Locate every uninfected red blood cell.
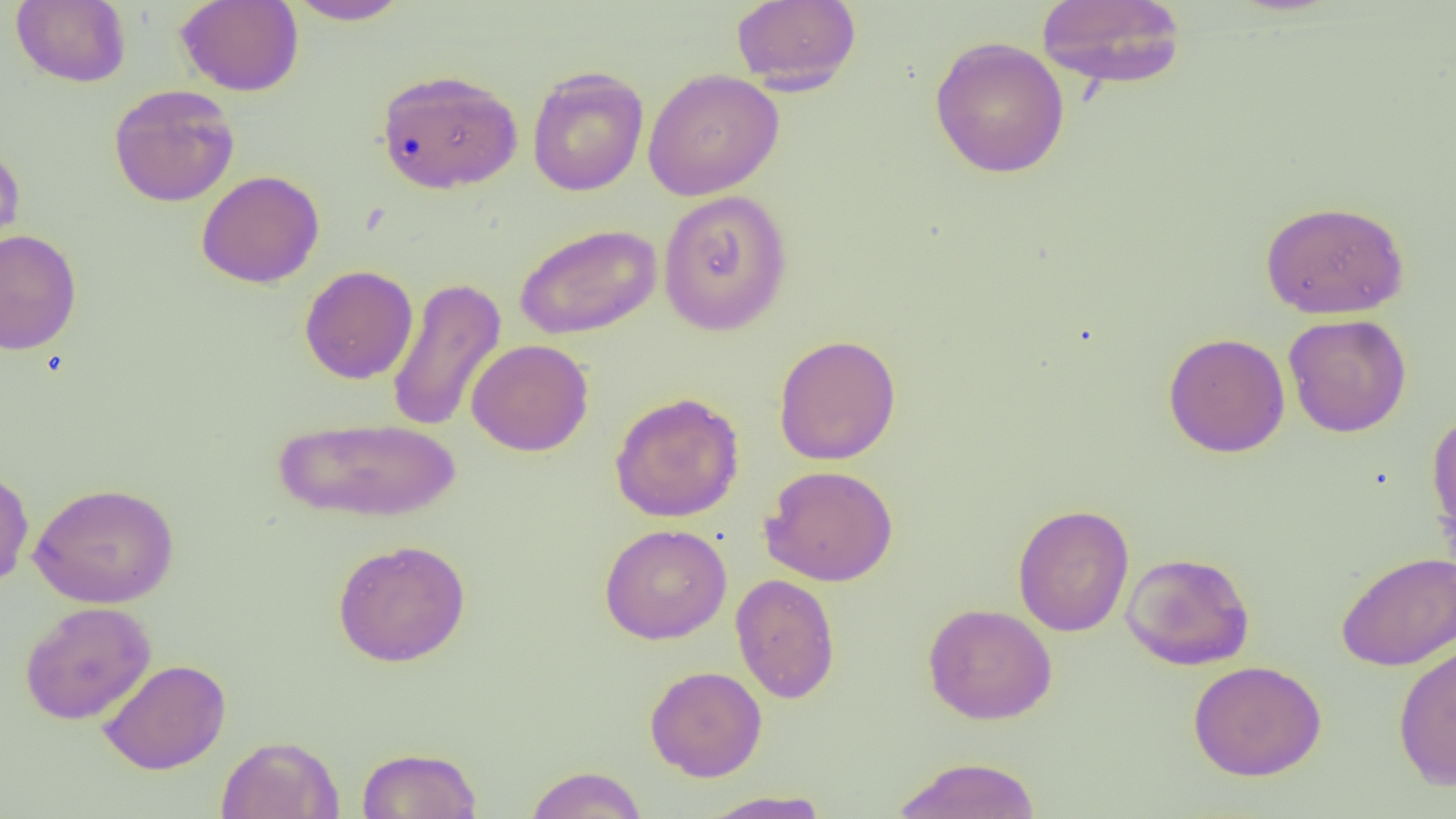
Approximate bounding boxes as (x1,y1)-(x2,y2) corner pairs in pixels.
Uninfected red blood cells: (11,0)-(131,88), (174,0)-(304,97), (284,0)-(413,25), (1035,0)-(1187,89), (731,1)-(861,92), (929,36)-(1070,179), (526,66)-(649,197), (376,68)-(523,195), (642,68)-(784,201), (108,84)-(240,207), (0,142)-(25,259), (196,170)-(325,288), (657,190)-(793,335), (1260,199)-(1410,319), (514,223)-(662,340), (0,229)-(83,356), (299,265)-(418,384), (386,276)-(506,434), (1283,313)-(1412,437), (1163,332)-(1291,457), (774,334)-(902,465), (466,338)-(594,457), (609,391)-(745,523), (1426,410)-(1456,547), (273,416)-(463,523), (0,464)-(35,590), (759,465)-(898,586), (28,481)-(179,608), (1012,504)-(1134,637), (599,523)-(732,644), (332,539)-(471,667), (1121,551)-(1255,670), (1335,551)-(1456,671), (730,573)-(841,704), (19,601)-(156,725), (923,602)-(1058,725), (1392,639)-(1456,790), (97,658)-(231,775), (1188,659)-(1327,781), (645,665)-(767,781), (216,735)-(343,818), (357,746)-(483,818), (891,756)-(1043,818), (524,765)-(648,819), (699,790)-(831,818).

slide-level diagnosis = negative for blood parasites
image size = 1456×819 pixels
modality = optical microscopy
magnification = 1000x
preparation = thin blood film
field of view = single